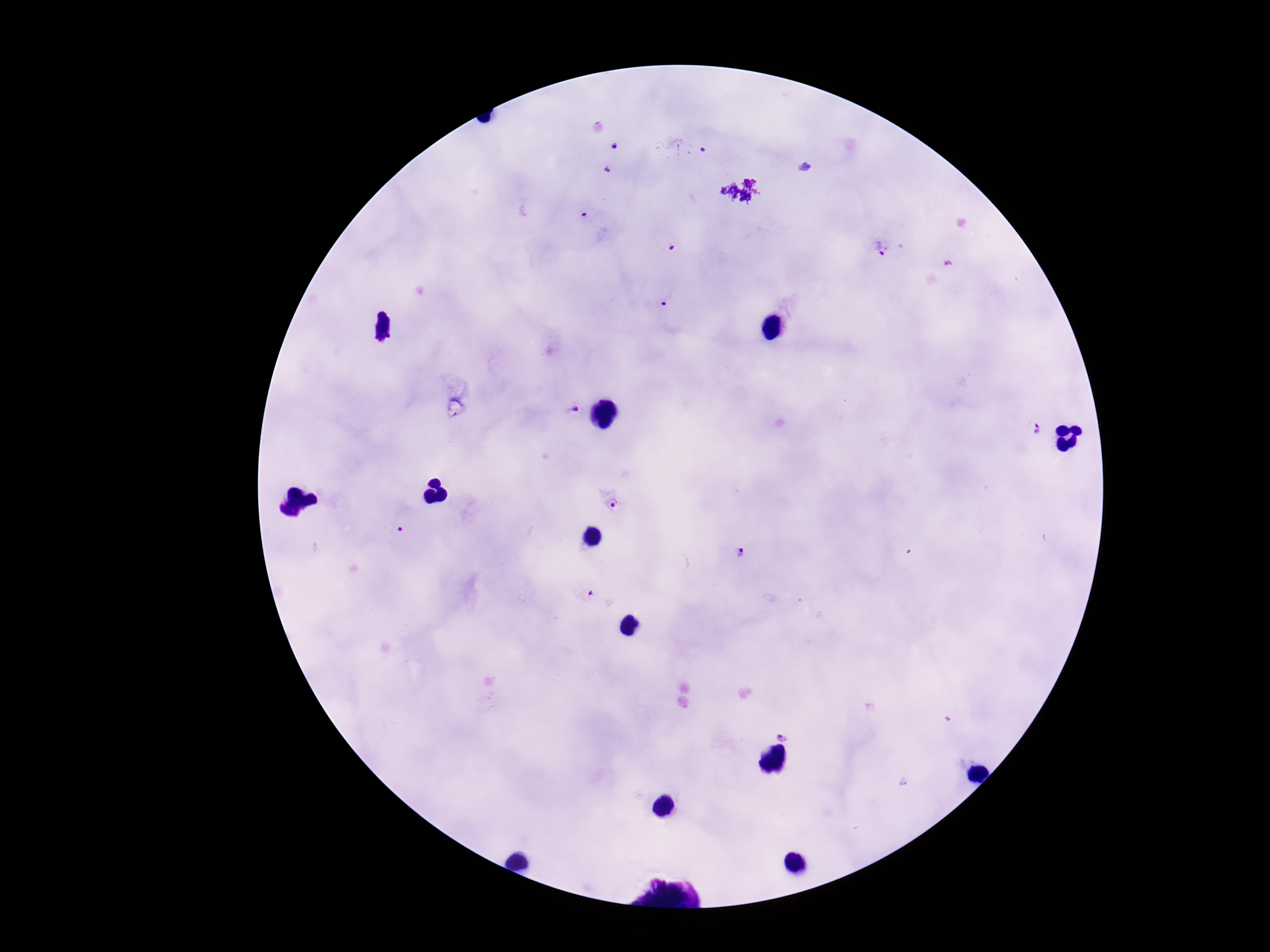
stain = Giemsa
image size = 1270×952 pixels
patient malaria status = infected
Plasmodium parasite locations = approximate object centers, in pixels from the top-left corner: (x=615, y=144), (x=706, y=149), (x=609, y=169), (x=585, y=213), (x=673, y=245), (x=883, y=246), (x=666, y=303), (x=572, y=410), (x=1038, y=430), (x=615, y=504), (x=400, y=529), (x=741, y=552), (x=588, y=596), (x=784, y=735)
preparation = thick blood film
magnification = 100x
capture = smartphone camera through the microscope eyepiece
field of view = one from this slide